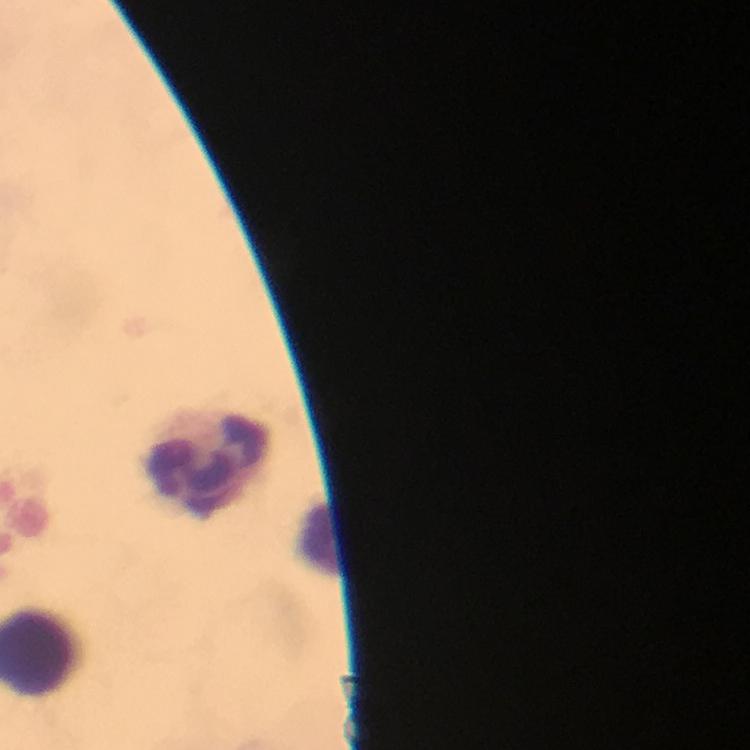
Approximate object centers, in pixels from the top-left corner.
Summary:
  - Leukocyte locations: (x=205, y=461)
  - Context: from a diagnostic examination for malaria
  - Cropped from: one field of view
  - Stain: Giemsa
  - Capture: smartphone camera through the microscope
  - Malaria parasites: none detected
  - Magnification: 100x
  - Preparation: thick smear
  - Image size: 750×750 pixels
  - Immersion oil: applied